Report the malaria status of this cell.
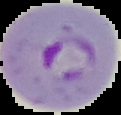
Parasitized.

image type = segmented cell region on a black background
preparation = thin blood film
image size = 121×115 pixels